Name the blood parasite species.
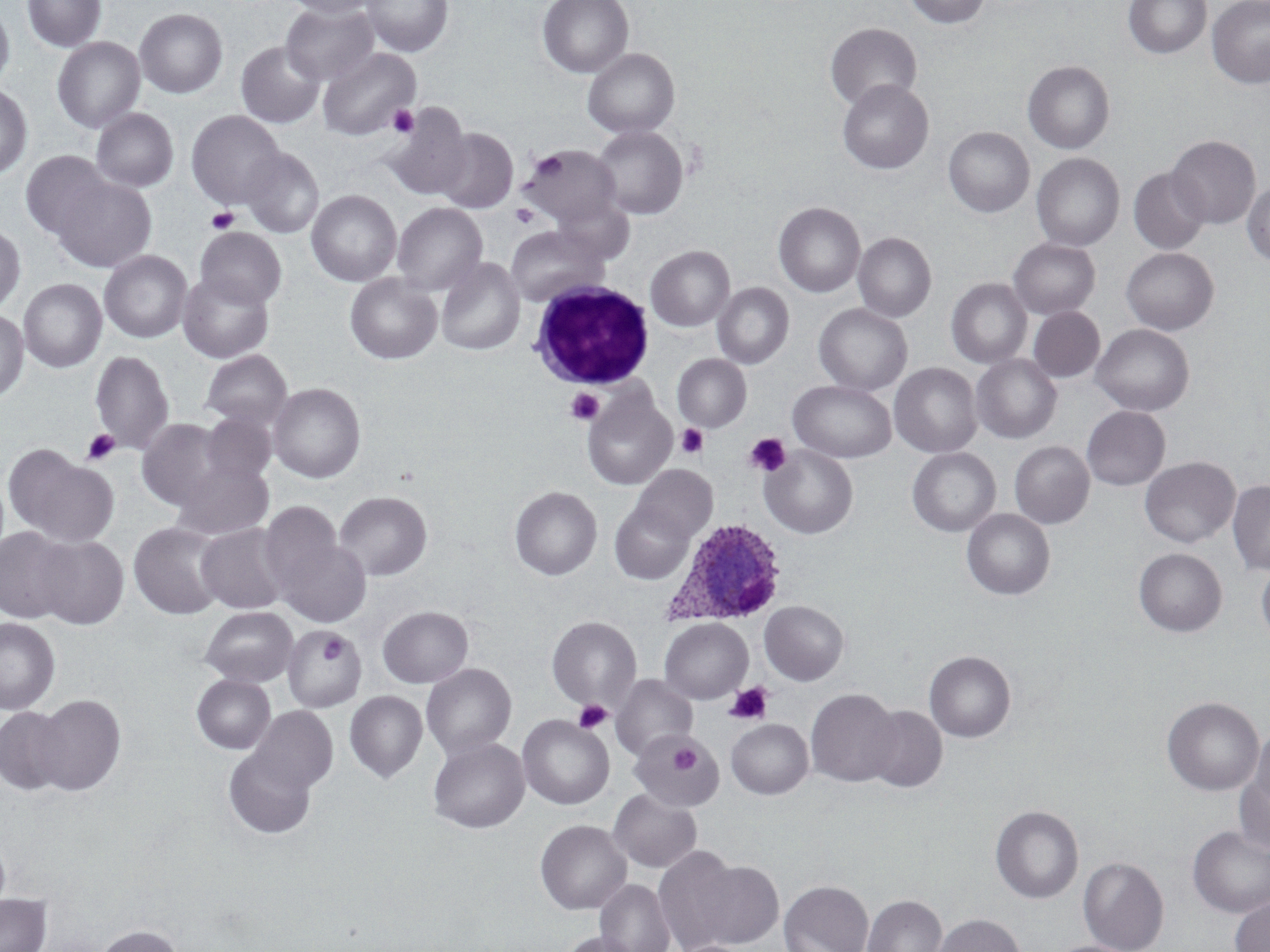
Plasmodium ovale.

modality = optical microscopy
Plasmodium ovale-infected red blood cell locations = approximate bounding boxes as [x1, y1, x2, y2] in pixels: [663, 518, 788, 627]
white blood cell locations = approximate bounding boxes as [x1, y1, x2, y2] in pixels: [528, 281, 655, 390]
magnification = 1000x
preparation = thin blood film
platelet locations = approximate bounding boxes as [x1, y1, x2, y2] in pixels: [387, 105, 420, 138], [532, 152, 567, 184], [510, 204, 540, 229], [206, 207, 240, 234], [565, 387, 604, 425], [677, 424, 709, 458], [81, 428, 120, 466], [745, 433, 792, 476], [320, 632, 349, 664], [725, 682, 773, 725], [574, 699, 613, 733], [670, 742, 700, 775]
uninfected red blood cell locations = approximate bounding boxes as [x1, y1, x2, y2] in pixels: [22, 0, 107, 53], [282, 0, 382, 18], [362, 0, 452, 58], [537, 0, 634, 78], [904, 0, 990, 29], [1123, 0, 1211, 59], [1207, 0, 1270, 88], [281, 3, 380, 86], [0, 4, 15, 89], [134, 8, 228, 98], [825, 23, 922, 110], [52, 37, 146, 133], [236, 40, 325, 129], [318, 46, 422, 140], [582, 48, 680, 139], [1023, 61, 1115, 154], [837, 79, 933, 174], [0, 83, 33, 179], [380, 103, 472, 200], [91, 108, 179, 193], [186, 110, 286, 209], [592, 125, 688, 220], [943, 127, 1034, 217], [434, 128, 518, 213], [1166, 135, 1261, 229], [521, 145, 622, 227], [240, 147, 325, 239], [20, 151, 112, 240], [1031, 153, 1125, 251], [1129, 168, 1210, 254], [51, 175, 158, 272], [1243, 181, 1270, 266], [306, 189, 402, 287], [553, 195, 635, 265], [392, 202, 488, 297], [774, 202, 866, 298], [0, 222, 26, 315], [505, 225, 609, 306], [195, 227, 288, 311], [853, 232, 936, 323], [1008, 238, 1100, 319], [646, 245, 735, 331], [1122, 247, 1219, 335], [99, 250, 192, 344], [435, 256, 525, 355], [177, 269, 275, 363], [344, 273, 442, 364], [946, 278, 1033, 369], [18, 279, 107, 373], [712, 282, 794, 369], [814, 303, 912, 396], [1028, 307, 1105, 382], [0, 310, 29, 403], [1091, 324, 1194, 416], [90, 348, 175, 457], [199, 349, 293, 431], [672, 354, 751, 432], [971, 354, 1061, 444], [890, 362, 982, 458], [787, 380, 896, 463], [267, 382, 366, 483], [582, 389, 677, 490], [1081, 406, 1170, 490], [201, 412, 276, 486], [137, 418, 234, 512], [1009, 441, 1094, 528], [5, 444, 119, 546], [759, 445, 859, 539], [907, 447, 1000, 536], [1139, 457, 1240, 548], [169, 458, 274, 542], [631, 465, 717, 545], [1227, 481, 1270, 575], [509, 486, 602, 580], [333, 491, 432, 581], [609, 500, 695, 584], [258, 503, 349, 605], [962, 509, 1055, 600], [128, 520, 228, 619], [196, 524, 290, 614], [0, 527, 75, 624], [272, 533, 372, 627], [32, 535, 129, 629], [1133, 548, 1227, 636], [1256, 558, 1270, 647], [759, 601, 849, 685], [200, 606, 298, 686], [377, 606, 473, 688], [547, 615, 641, 710], [0, 617, 60, 714], [659, 618, 753, 704], [281, 625, 367, 713], [924, 651, 1016, 742], [421, 663, 517, 761], [191, 673, 276, 754], [611, 675, 698, 761], [806, 688, 901, 787], [344, 690, 428, 783], [29, 694, 126, 796], [1162, 696, 1264, 795], [864, 705, 948, 793], [0, 707, 69, 795], [248, 707, 337, 795], [518, 715, 614, 809], [726, 719, 813, 799], [1248, 726, 1270, 817], [628, 730, 724, 811], [428, 736, 530, 833], [222, 747, 318, 839], [1234, 759, 1270, 856], [608, 789, 702, 872], [991, 805, 1083, 903], [535, 819, 632, 915], [1187, 826, 1270, 918], [0, 835, 11, 916], [652, 846, 750, 952], [1078, 856, 1169, 952], [686, 858, 784, 948], [595, 879, 676, 952], [779, 879, 874, 952], [0, 893, 52, 952], [863, 894, 946, 952], [1230, 896, 1270, 952], [931, 913, 1026, 952], [95, 924, 184, 952], [558, 931, 642, 952]
field of view = single
stain = May-Grünwald-Giemsa
image size = 1270×952 pixels